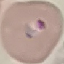
malaria status = parasitized
capture = smartphone through the microscope eyepiece
image type = cell patch, automatically extracted from a larger field of view and resized to 64 × 64 pixels
preparation = thin smear
stain = Giemsa